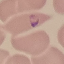 Malaria status: parasitized. Thin blood film. Giemsa-stained preparation. Acquired by smartphone through the microscope eyepiece. Automatically extracted cell patch, resized to 64 × 64 pixels.